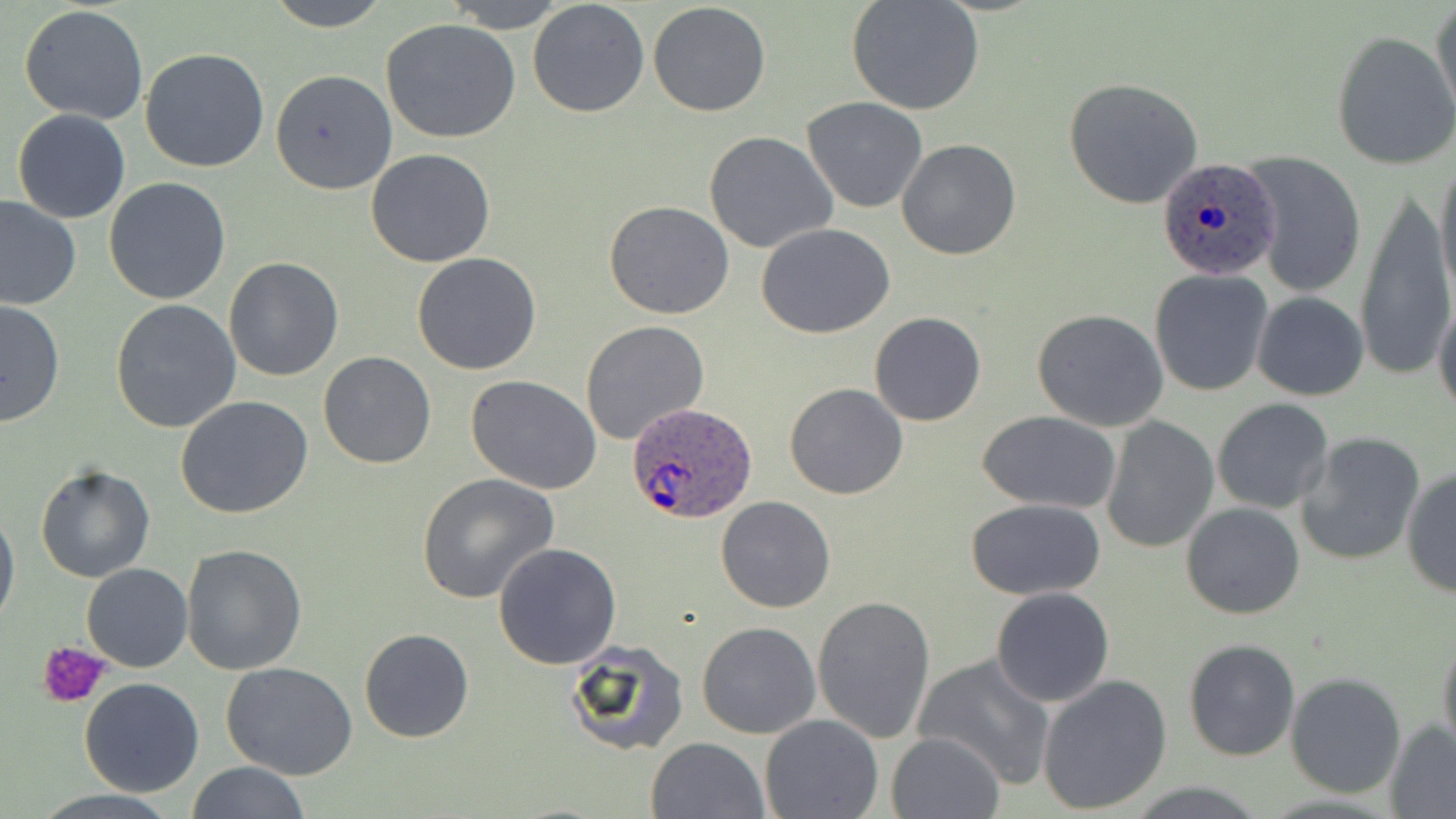

slide_level_diagnosis: Plasmodium ovale
preparation: thin blood smear
stain: May-Grünwald-Giemsa
platelet_locations: 'approximate bounding boxes as (x1,y1)-(x2,y2) corner pairs in pixels: (38,640)-(109,707)'
modality: optical microscopy
field_of_view: one of a larger specimen
image_size: 1456×819 pixels
uninfected_red_blood_cell_locations: 'approximate bounding boxes as (x1,y1)-(x2,y2) corner pairs in pixels: (264,0)-(391,31), (442,0)-(570,30), (528,0)-(650,118), (847,0)-(985,116), (1430,1)-(1455,128), (647,2)-(772,117), (19,5)-(149,126), (381,19)-(520,143), (1331,30)-(1456,170), (140,46)-(271,173), (269,69)-(398,195), (1062,77)-(1206,211), (801,96)-(928,213), (11,110)-(130,224), (7,115)-(100,309), (703,131)-(838,255), (897,137)-(1021,260), (366,147)-(496,267), (1240,150)-(1367,299), (1434,155)-(1455,306), (104,177)-(233,306), (1354,187)-(1453,383), (0,196)-(81,312), (604,201)-(733,320), (756,223)-(896,338), (412,252)-(543,376), (223,257)-(344,381), (1149,269)-(1274,395), (1433,290)-(1456,419), (1252,292)-(1369,401), (0,299)-(65,428), (109,300)-(242,433), (1031,308)-(1171,430), (868,312)-(988,426), (580,321)-(708,443), (317,351)-(437,470), (465,376)-(603,495), (784,383)-(909,499), (175,394)-(313,519), (1212,399)-(1334,515), (975,410)-(1123,512), (1099,418)-(1219,554), (1294,431)-(1426,566), (34,464)-(155,583), (1401,467)-(1455,596), (416,473)-(559,603), (715,495)-(836,613), (967,499)-(1106,600), (1182,501)-(1306,620), (0,502)-(19,633), (494,541)-(622,668), (182,544)-(309,676), (82,562)-(193,672), (990,588)-(1114,707), (811,594)-(937,745), (697,620)-(821,738), (358,628)-(474,744), (1437,633)-(1456,760), (562,638)-(690,758), (1182,638)-(1300,762), (914,654)-(1055,787), (221,662)-(358,781), (1287,671)-(1408,798), (1037,674)-(1172,814), (77,677)-(205,797), (760,714)-(885,819), (1385,721)-(1456,816), (887,732)-(1004,818), (646,737)-(769,819), (186,761)-(310,819)'
magnification: 1000x
plasmodium_ovale_infected_red_blood_cell_locations: 'approximate bounding boxes as (x1,y1)-(x2,y2) corner pairs in pixels: (1157,157)-(1280,280), (625,401)-(760,525)'